Find each cell and give its type.
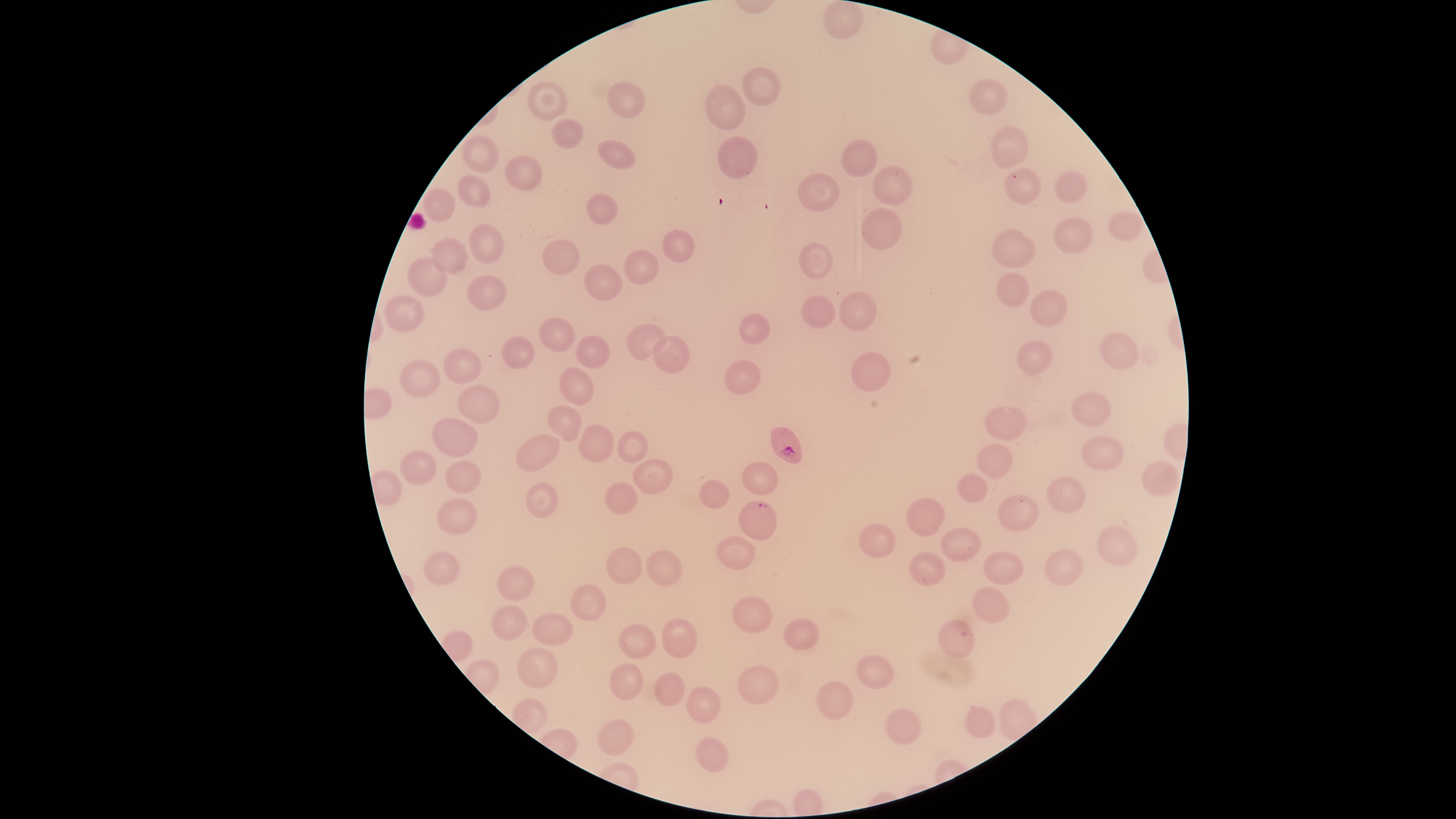

Approximate bounding boxes as [left, top, right, bottom] in pixels.
Parasitized RBCs: [770, 426, 803, 464], [737, 500, 777, 541].
Uninfected RBCs: [823, 0, 864, 40], [742, 67, 781, 106], [968, 78, 1008, 116], [527, 81, 568, 120], [607, 81, 646, 118], [704, 84, 746, 131], [551, 118, 584, 149], [990, 126, 1029, 170], [461, 135, 499, 172], [717, 136, 757, 179], [597, 139, 636, 169], [840, 139, 878, 178], [504, 155, 543, 191], [872, 165, 913, 206], [1004, 168, 1042, 205], [1054, 171, 1088, 203], [797, 173, 840, 212], [457, 174, 490, 208], [422, 188, 456, 222], [586, 193, 618, 225], [861, 207, 902, 251], [1107, 211, 1144, 243], [1053, 216, 1094, 254], [468, 223, 504, 264], [990, 228, 1035, 269], [661, 229, 695, 263], [430, 235, 470, 275], [542, 239, 580, 275], [798, 242, 833, 279], [624, 249, 660, 285], [407, 256, 447, 297], [583, 264, 623, 302], [995, 272, 1030, 308], [466, 275, 507, 311], [1029, 289, 1067, 327], [838, 291, 877, 332], [384, 294, 424, 333], [801, 294, 836, 329], [738, 313, 770, 345], [538, 317, 575, 352], [626, 323, 667, 360], [1099, 332, 1139, 369], [501, 335, 535, 369], [575, 335, 611, 368], [653, 335, 691, 374], [1016, 339, 1053, 376], [442, 347, 481, 384], [850, 351, 891, 393], [400, 359, 440, 397], [724, 360, 761, 396], [559, 367, 595, 406], [457, 385, 499, 425], [1071, 392, 1111, 427], [547, 405, 582, 442], [984, 405, 1027, 441], [431, 417, 478, 457], [578, 424, 613, 462], [617, 430, 648, 463], [515, 434, 560, 472], [1081, 435, 1125, 471], [976, 443, 1013, 479], [399, 450, 437, 485], [632, 458, 673, 494], [444, 460, 481, 494], [1141, 460, 1179, 497], [741, 461, 779, 495], [956, 473, 988, 504], [1046, 476, 1086, 514], [698, 479, 730, 510], [604, 481, 638, 515], [525, 482, 558, 518], [997, 494, 1040, 532], [436, 497, 477, 536], [906, 497, 945, 536], [858, 523, 896, 559], [1096, 526, 1139, 566], [940, 527, 981, 562], [716, 536, 756, 569], [606, 547, 642, 584], [1044, 549, 1084, 586], [646, 550, 683, 587], [423, 551, 460, 585], [983, 551, 1024, 585], [908, 552, 946, 587], [496, 564, 534, 602], [570, 584, 606, 621], [972, 587, 1010, 624], [732, 596, 772, 633], [491, 605, 527, 640], [531, 612, 574, 646], [662, 618, 697, 658], [783, 618, 820, 651], [937, 619, 976, 659], [619, 623, 656, 660], [517, 647, 559, 689], [856, 654, 895, 689], [610, 662, 643, 700], [737, 664, 780, 704], [654, 672, 686, 706], [816, 680, 854, 720], [686, 686, 721, 724], [964, 705, 996, 738], [884, 707, 922, 745], [597, 718, 635, 756], [696, 736, 729, 773].
No WBCs identified.

Giemsa-stained preparation. Image is 1456×819 pixels. Circular visible region. Thin blood smear. One field of view of the specimen. Species: Plasmodium falciparum. Photographed with a smartphone camera through the microscope eyepiece.